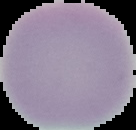

Summary:
  - Malaria status: uninfected
  - Image type: segmented cell region on a black background
  - Image size: 136×130 pixels
  - Preparation: thin blood smear